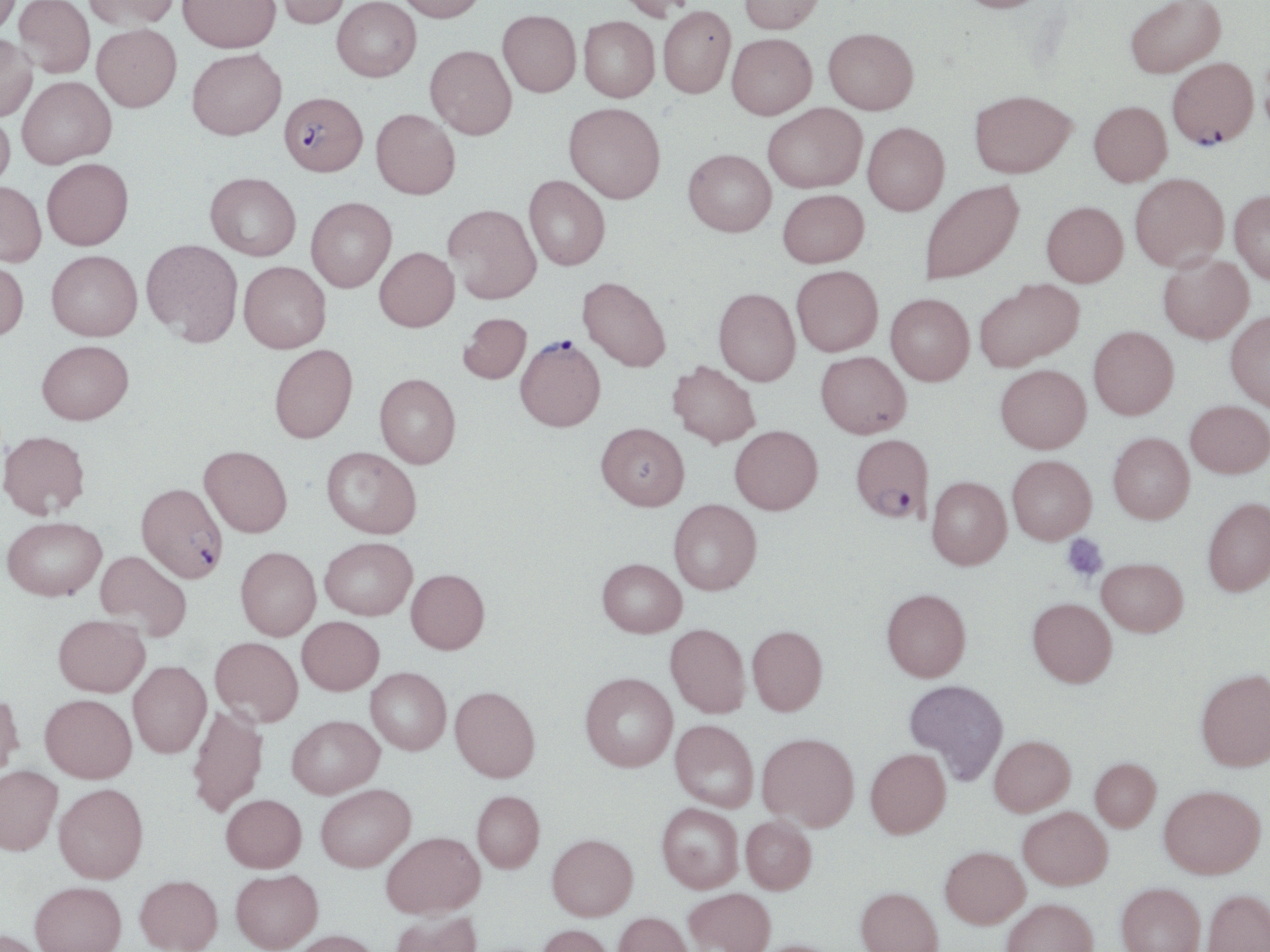

Approximate bounding boxes as (x1, y1, x2, y2) in pixels. Plasmodium falciparum-infected red blood cell locations: (1167, 58, 1258, 148), (279, 92, 367, 176), (515, 337, 605, 432), (851, 434, 934, 524), (136, 482, 227, 582). Platelet locations: (1062, 534, 1109, 581). Uninfected red blood cell locations: (0, 0, 21, 36), (13, 0, 95, 78), (83, 0, 179, 30), (178, 0, 281, 52), (270, 0, 350, 29), (331, 0, 421, 82), (395, 0, 486, 21), (616, 0, 698, 21), (738, 0, 825, 34), (952, 0, 1053, 13), (1125, 0, 1226, 78), (658, 6, 736, 98), (497, 9, 581, 97), (578, 16, 660, 102), (92, 24, 182, 112), (823, 27, 918, 114), (0, 34, 37, 122), (727, 34, 817, 119), (425, 45, 517, 139), (187, 48, 286, 140), (17, 76, 116, 168), (969, 89, 1076, 178), (1088, 101, 1172, 186), (564, 102, 665, 203), (763, 103, 866, 193), (371, 109, 460, 199), (0, 111, 15, 192), (862, 122, 949, 215), (683, 149, 776, 236), (42, 158, 134, 250), (205, 172, 301, 260), (1130, 173, 1229, 271), (524, 175, 610, 270), (0, 181, 46, 267), (919, 181, 1024, 284), (777, 189, 869, 267), (1230, 189, 1270, 285), (306, 197, 396, 292), (1041, 201, 1128, 287), (443, 204, 541, 303), (141, 239, 242, 344), (374, 247, 459, 331), (47, 250, 142, 340), (1158, 253, 1254, 344), (0, 257, 29, 342), (239, 261, 331, 352), (791, 265, 883, 356), (577, 275, 671, 372), (974, 278, 1083, 371), (713, 288, 800, 385), (886, 294, 974, 385), (1226, 309, 1270, 411), (458, 313, 532, 384), (1089, 326, 1178, 419), (37, 340, 133, 424), (269, 344, 358, 443), (816, 351, 911, 438), (667, 360, 761, 448), (995, 365, 1091, 453), (375, 373, 461, 468), (1186, 400, 1270, 478), (596, 422, 689, 510), (730, 425, 822, 514), (0, 430, 90, 519), (1108, 433, 1194, 523), (199, 445, 292, 537), (322, 446, 421, 538), (1007, 455, 1096, 544), (926, 476, 1012, 569), (1203, 497, 1270, 596), (669, 499, 761, 595), (2, 516, 106, 601), (320, 537, 417, 620), (235, 547, 320, 640), (96, 550, 192, 640), (1097, 557, 1188, 636), (597, 558, 686, 637), (406, 568, 490, 654), (882, 588, 971, 682), (1028, 597, 1116, 687), (53, 614, 150, 697), (297, 616, 384, 694), (666, 623, 750, 717), (747, 625, 827, 715), (210, 636, 303, 726), (128, 661, 211, 758), (366, 667, 451, 755), (1195, 668, 1270, 770), (580, 672, 678, 771), (904, 679, 1009, 784), (450, 686, 540, 782), (0, 690, 24, 781), (40, 693, 137, 783), (187, 704, 268, 818), (287, 715, 384, 798), (670, 720, 759, 812), (758, 732, 859, 830), (989, 735, 1076, 816), (865, 748, 951, 838), (1090, 757, 1161, 831), (0, 765, 62, 855), (54, 783, 148, 883), (316, 784, 415, 872), (1159, 785, 1265, 879), (472, 790, 545, 873), (221, 794, 306, 872), (657, 803, 744, 892), (1018, 806, 1112, 889), (741, 815, 817, 894), (382, 831, 484, 917), (547, 834, 638, 920), (940, 845, 1030, 928), (231, 869, 323, 951), (135, 874, 223, 952), (30, 881, 126, 952), (1116, 882, 1205, 952), (856, 886, 943, 952), (684, 888, 775, 952), (1203, 888, 1270, 952), (1001, 897, 1098, 952), (389, 910, 482, 952), (613, 911, 695, 952), (536, 924, 616, 952), (0, 928, 47, 952), (290, 930, 381, 952), (750, 939, 845, 952). Slide-level diagnosis: Plasmodium falciparum. Single field of view. Light microscopy. 1000x magnification. Image is 1270×952 pixels. May-Grünwald-Giemsa-stained preparation. Thin blood smear.